Assess this cell for malaria.
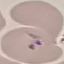
It is uninfected.

capture = smartphone camera at the microscope eyepiece
preparation = thin smear
image type = cell patch, automatically extracted from a larger field of view and resized to 64 × 64 pixels
stain = Giemsa